Report the malaria status of this cell.
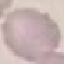
Uninfected.

stain = Giemsa
capture = smartphone camera at the microscope eyepiece
preparation = thin blood film
image type = cell patch, automatically extracted from a larger field of view and resized to 64 × 64 pixels